Give the preparation type.
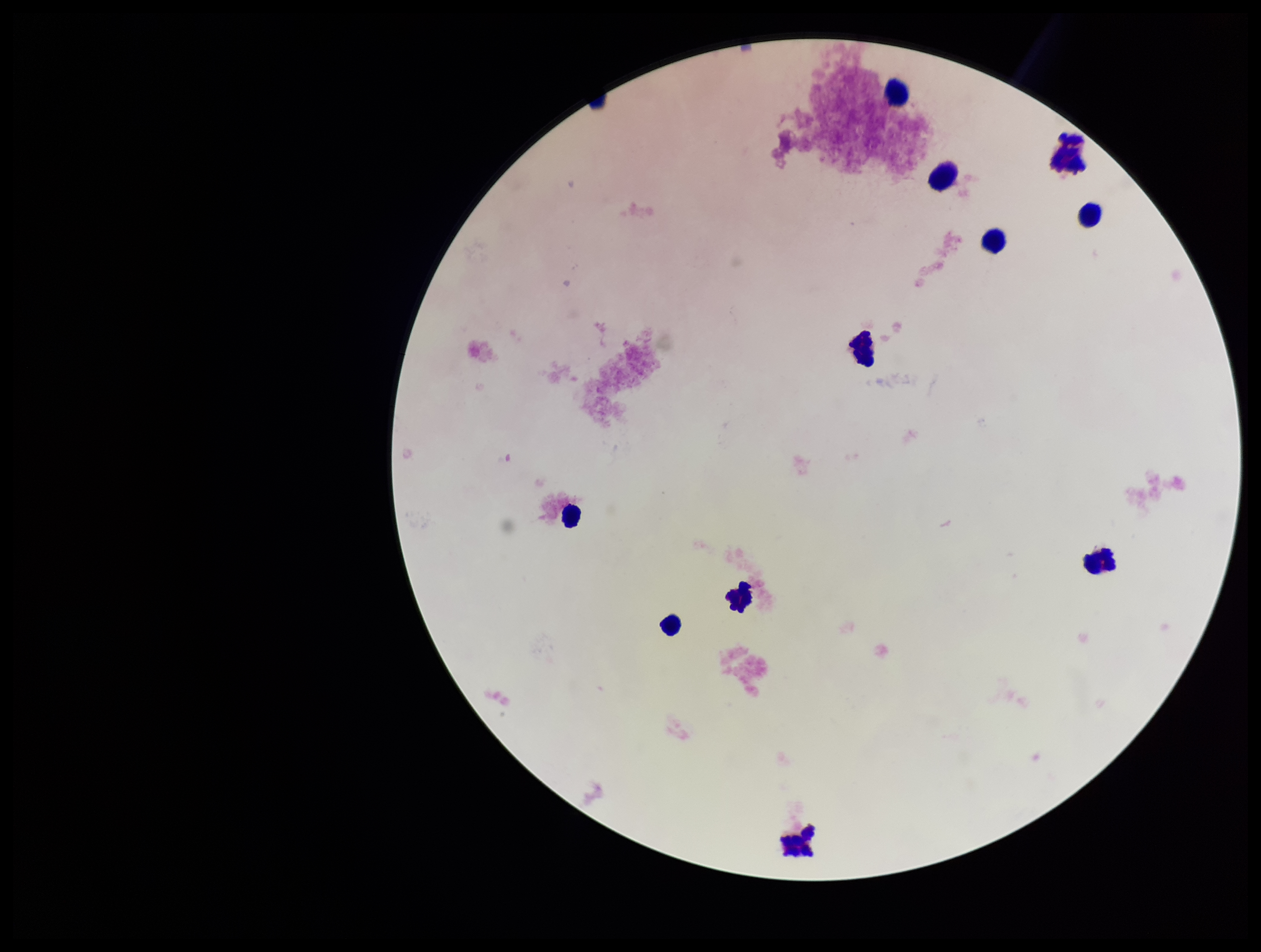

Thick.

leukocyte_count: 11
field_of_view: single
image_size: 1261×952 pixels
capture: smartphone photograph through the microscope eyepiece
stain: Giemsa
parasite_count: 0
patient_malaria_status: negative
plasmodium_parasites: none identified